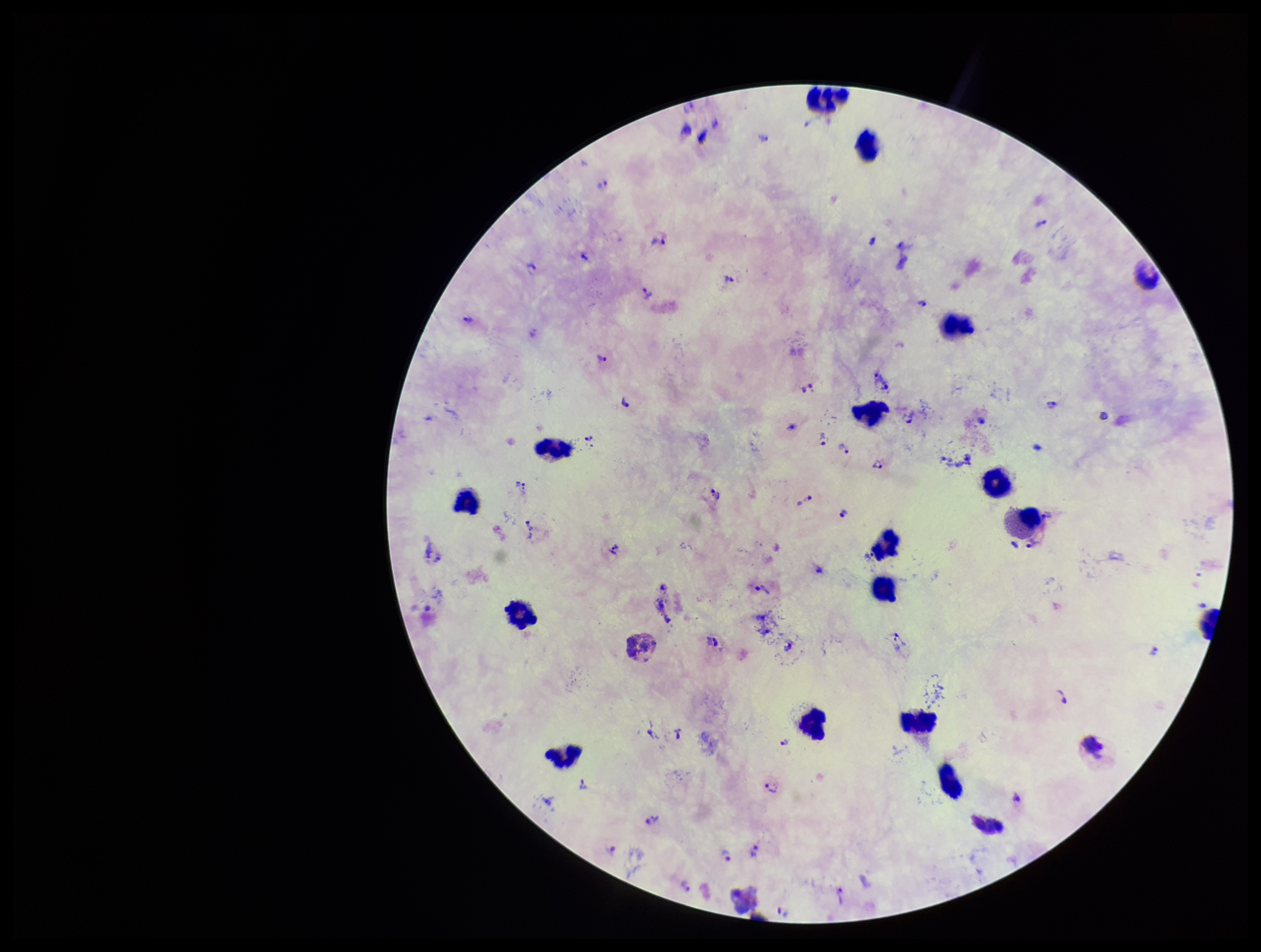

Patient malaria status: infected. Leukocyte count: 16. Image is 1261×952 pixels. Preparation: thick smear. Stained with Giemsa. Plasmodium parasites: detected. Parasite count: 34. One field from this slide. Smartphone photograph taken through the eyepiece of a microscope. Species reported for this patient: Plasmodium vivax.